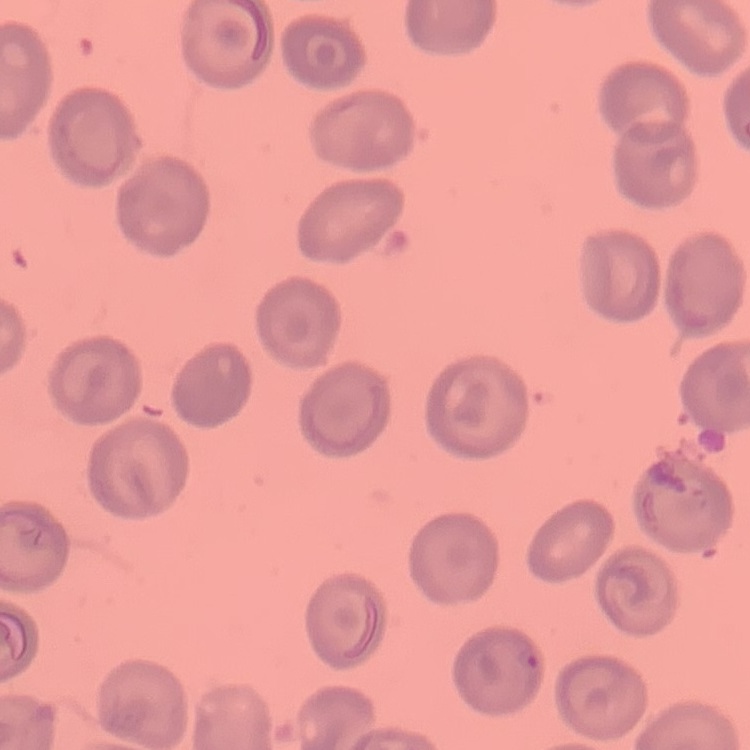

erythrocyte morphology = no rouleaux formation
preparation = thin peripheral smear
stain = Field's or Giemsa
image type = square crop of a larger photomicrograph